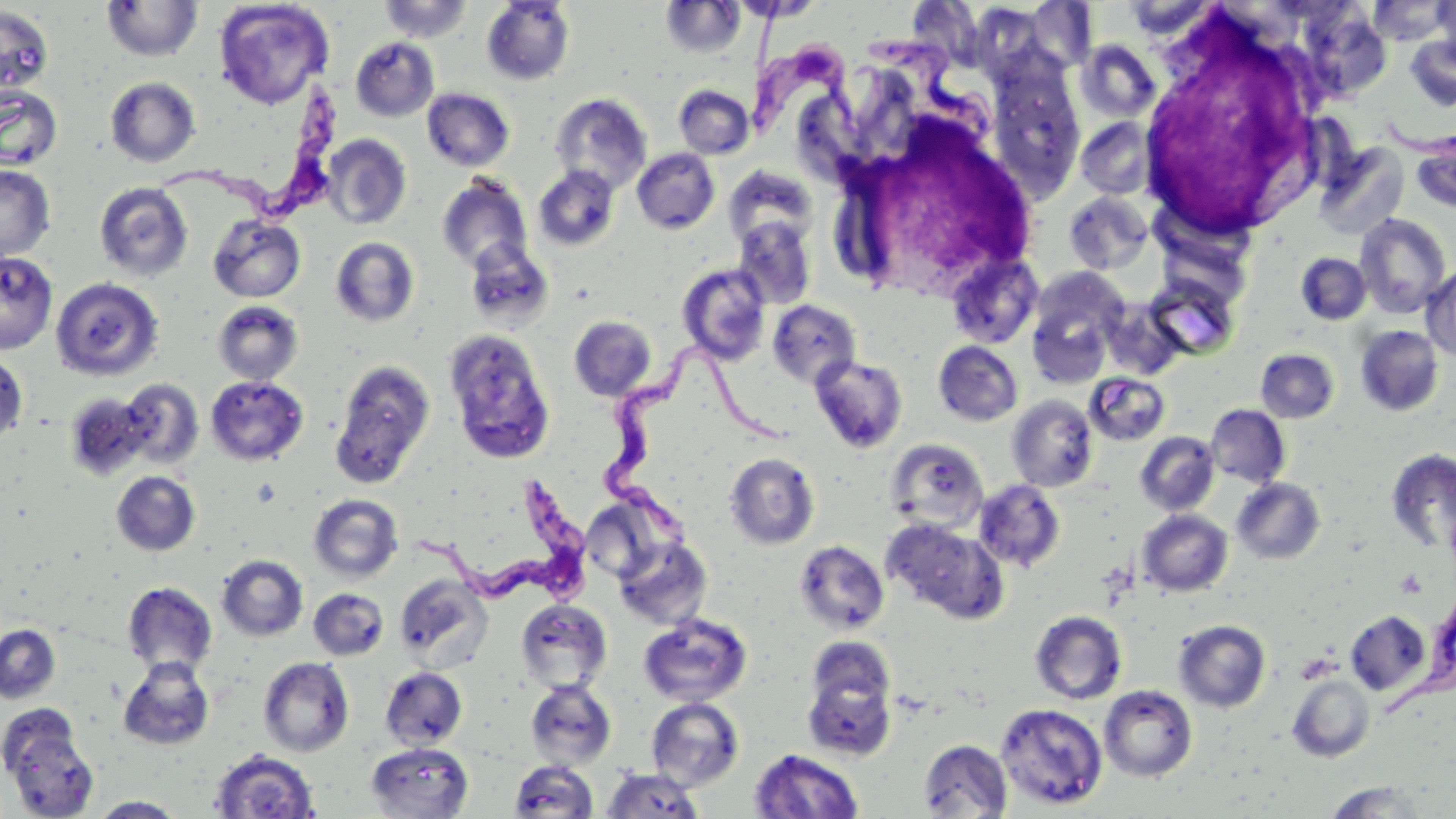

Summary:
  - Coordinate format: approximate bounding boxes as (x1,y1)-(x2,y2) corner pairs in pixels
  - Uninfected red blood cell locations: (213,0)-(334,110), (377,0)-(475,43), (660,0)-(746,58), (1433,0)-(1456,66), (101,1)-(203,62), (481,1)-(575,85), (1121,1)-(1219,43), (1366,1)-(1452,45), (0,4)-(54,98), (1024,4)-(1097,73), (1293,6)-(1392,101), (1405,35)-(1456,111), (351,37)-(439,122), (1077,40)-(1161,123), (986,63)-(1088,204), (105,76)-(201,167), (0,85)-(62,170), (674,85)-(754,159), (422,88)-(514,172), (550,93)-(652,194), (1076,117)-(1156,200), (321,134)-(412,230), (1412,134)-(1456,215), (1313,142)-(1409,240), (632,148)-(720,234), (0,164)-(55,261), (533,166)-(619,251), (723,166)-(818,249), (437,174)-(532,272), (94,182)-(194,282), (1063,191)-(1154,276), (1354,213)-(1452,319), (208,214)-(305,302), (733,218)-(816,309), (1157,219)-(1251,302), (330,236)-(420,327), (463,240)-(555,330), (0,252)-(59,354), (1295,252)-(1371,324), (946,254)-(1043,349), (677,264)-(771,365), (1420,265)-(1456,361), (1025,271)-(1127,385), (1144,275)-(1240,359), (50,277)-(164,381), (767,299)-(860,389), (212,300)-(304,385), (1101,302)-(1184,379), (569,315)-(657,401), (1354,325)-(1444,416), (443,329)-(555,464), (933,341)-(1023,426), (1256,348)-(1339,423), (0,352)-(28,444), (810,356)-(908,453), (330,360)-(436,487), (1085,372)-(1170,446), (205,375)-(309,466), (119,378)-(204,469), (63,392)-(153,481), (1007,395)-(1098,492), (1205,404)-(1291,488), (1135,432)-(1220,515), (886,439)-(988,532), (1386,449)-(1456,554), (724,452)-(820,549), (111,470)-(201,556), (1232,478)-(1326,564), (974,480)-(1066,572), (309,494)-(403,583), (591,506)-(660,578), (1137,510)-(1233,597), (882,519)-(1008,624), (613,535)-(712,629), (795,541)-(890,634), (217,555)-(308,641), (394,573)-(493,671), (122,581)-(217,676), (308,588)-(389,660), (515,600)-(612,692), (1030,610)-(1128,704), (1345,610)-(1431,695), (639,613)-(752,707), (1173,619)-(1271,713), (0,624)-(61,704), (807,635)-(896,714), (258,656)-(354,757), (118,658)-(214,750), (380,667)-(468,750), (802,670)-(897,761), (1287,674)-(1375,762), (525,679)-(616,770), (1099,685)-(1198,782), (646,697)-(744,791), (995,703)-(1108,810), (3,722)-(99,819), (918,739)-(1013,817), (367,742)-(473,818), (209,749)-(320,818), (749,749)-(865,818), (510,760)-(599,817), (601,767)-(704,818), (1322,781)-(1430,817), (88,796)-(188,817)
  - White blood cell locations: (1148,29)-(1327,230), (873,131)-(1042,296)
  - Trypanosoma brucei locations: (744,33)-(866,143), (869,39)-(997,145), (142,73)-(343,231), (603,340)-(780,536), (425,478)-(594,607)
  - Slide-level diagnosis: Trypanosoma brucei
  - Magnification: 1000x
  - Image size: 1456×819 pixels
  - Stain: May-Grünwald-Giemsa
  - Modality: optical microscopy
  - Preparation: thin blood film
  - Field of view: one of a larger specimen